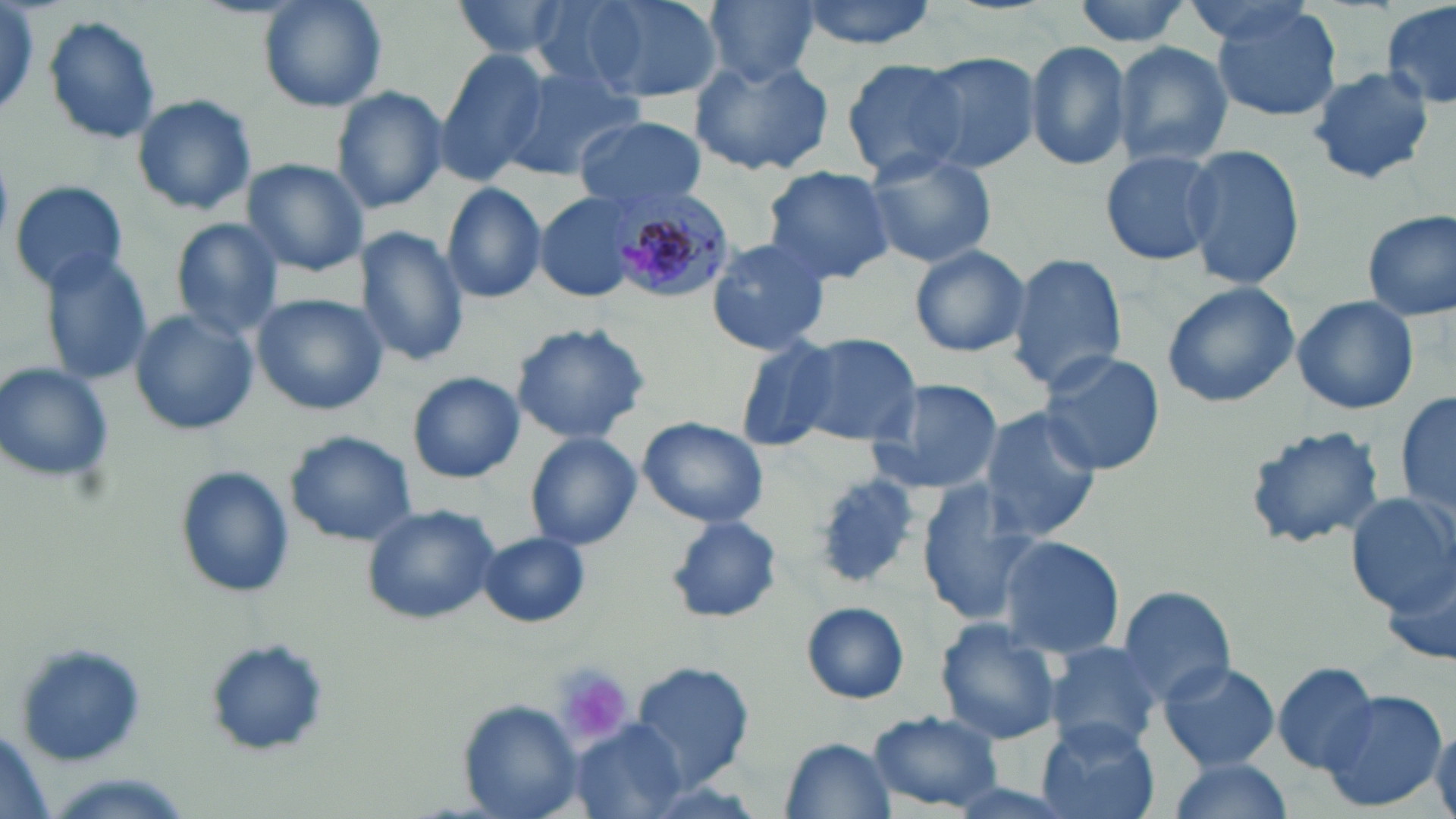
{
  "slide_level_diagnosis": "Plasmodium malariae",
  "magnification": "1000x",
  "modality": "optical microscopy",
  "uninfected_red_blood_cell_locations": "approximate bounding boxes as (x1,y1)-(x2,y2) corner pairs in pixels: (0,0)-(47,123), (259,0)-(387,112), (445,0)-(584,63), (529,0)-(655,97), (574,0)-(719,104), (794,0)-(940,50), (1070,0)-(1197,48), (702,1)-(824,86), (1179,1)-(1321,46), (1383,2)-(1456,114), (1208,3)-(1346,124), (39,17)-(164,147), (1024,40)-(1132,172), (1110,41)-(1234,171), (435,49)-(552,182), (915,52)-(1041,173), (688,54)-(836,178), (841,58)-(968,179), (499,63)-(641,181), (1307,65)-(1435,186), (331,87)-(448,213), (130,93)-(256,216), (575,116)-(706,209), (1096,145)-(1224,265), (1180,145)-(1306,293), (862,149)-(998,270), (242,158)-(370,278), (760,165)-(895,285), (8,179)-(130,294), (441,181)-(547,305), (535,193)-(643,303), (1361,210)-(1455,322), (171,218)-(285,339), (354,227)-(470,366), (704,235)-(835,355), (910,245)-(1031,358), (39,251)-(153,388), (1006,252)-(1128,396), (1160,282)-(1300,409), (251,293)-(386,415), (1292,294)-(1420,416), (128,308)-(259,435), (512,322)-(651,444), (788,331)-(923,448), (725,333)-(842,449), (1035,349)-(1166,475), (0,362)-(116,485), (407,371)-(524,483), (863,378)-(1004,496), (1396,387)-(1454,530), (978,408)-(1102,539), (637,416)-(768,528), (1243,423)-(1388,551), (285,432)-(416,547), (523,432)-(644,550), (174,467)-(293,597), (915,484)-(1038,629), (1346,491)-(1454,611), (361,504)-(498,624), (667,516)-(781,624), (479,532)-(591,627), (995,535)-(1125,661), (1382,558)-(1456,670), (1118,585)-(1238,708), (802,602)-(909,703), (933,620)-(1063,745), (204,640)-(330,758), (13,641)-(151,769), (1040,642)-(1162,750), (1157,659)-(1280,771), (631,660)-(756,785), (1271,661)-(1382,773), (1317,687)-(1448,812), (464,702)-(582,816), (870,710)-(1003,811), (1034,721)-(1161,819), (567,722)-(689,818), (1429,722)-(1456,818), (0,725)-(54,819), (781,736)-(896,818), (1164,757)-(1295,819)",
  "plasmodium_malariae_infected_red_blood_cell_locations": "approximate bounding boxes as (x1,y1)-(x2,y2) corner pairs in pixels: (612,191)-(736,304)",
  "image_size": "1456×819 pixels",
  "platelet_locations": "approximate bounding boxes as (x1,y1)-(x2,y2) corner pairs in pixels: (552,664)-(636,745)",
  "field_of_view": "one of a larger specimen",
  "preparation": "thin blood film",
  "stain": "May-Grünwald-Giemsa"
}